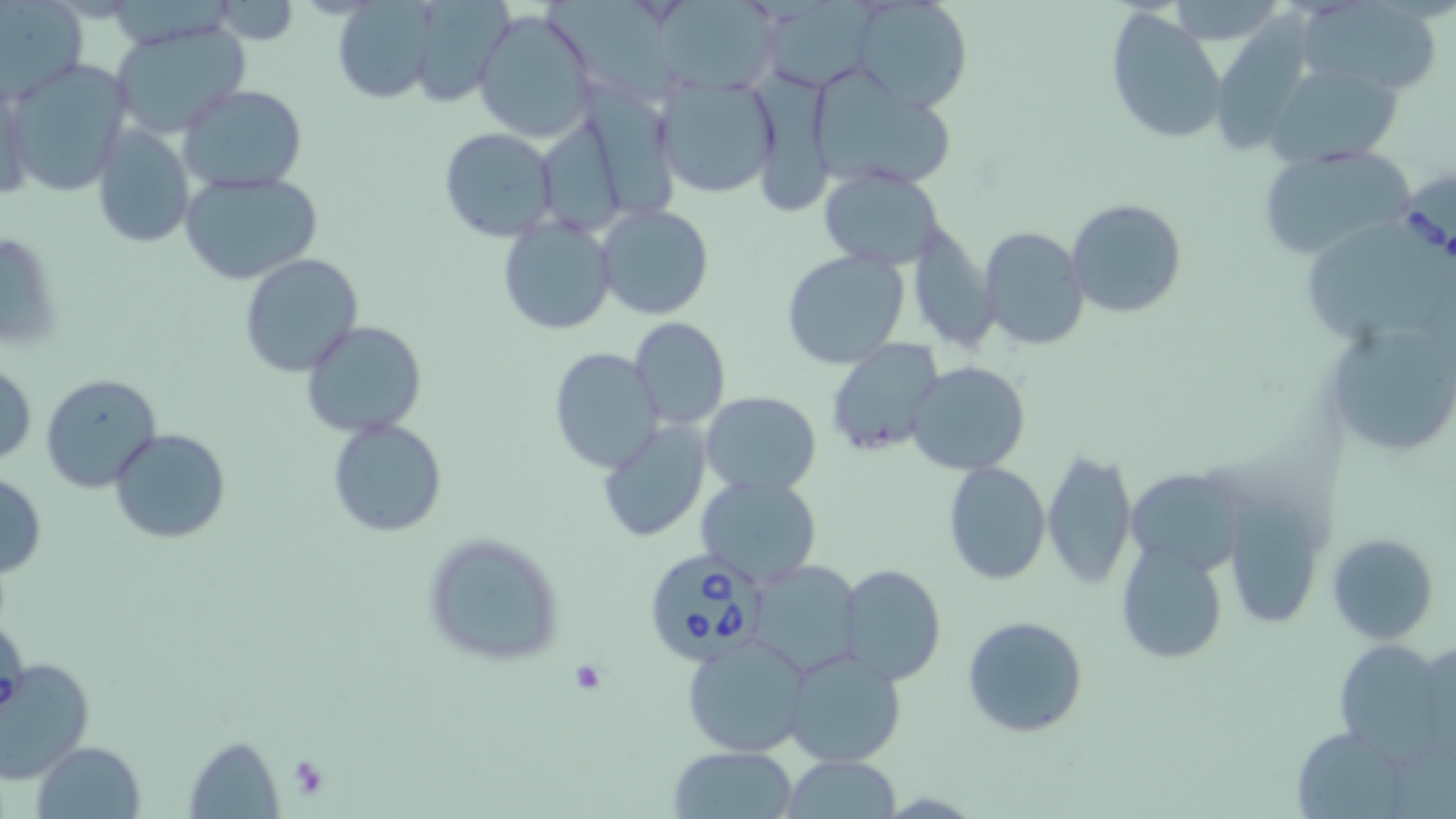
Approximate bounding boxes as (x1, y1, x2, y2) in pixels. Platelet locations: (569, 660, 607, 696), (286, 753, 331, 800). Babesia divergens-infected red blood cell locations: (1399, 173, 1455, 280), (644, 548, 771, 665). Uninfected red blood cell locations: (407, 0, 510, 108), (539, 0, 683, 97), (771, 0, 893, 89), (213, 1, 300, 46), (652, 1, 788, 94), (854, 1, 972, 111), (1, 2, 87, 103), (330, 2, 438, 103), (1162, 2, 1287, 41), (1300, 2, 1443, 96), (472, 7, 598, 142), (1104, 7, 1230, 145), (109, 17, 251, 139), (5, 60, 132, 196), (1268, 62, 1400, 166), (750, 68, 849, 218), (806, 70, 958, 193), (654, 73, 783, 200), (2, 78, 34, 209), (178, 84, 308, 193), (584, 84, 688, 220), (91, 123, 195, 248), (439, 127, 558, 242), (1256, 144, 1414, 260), (818, 168, 946, 269), (178, 169, 324, 286), (1064, 199, 1186, 320), (595, 204, 714, 320), (498, 216, 615, 336), (906, 220, 999, 352), (978, 226, 1089, 351), (1, 227, 61, 353), (781, 249, 909, 369), (240, 254, 363, 376), (628, 316, 731, 431), (1320, 316, 1456, 460), (301, 321, 426, 438), (827, 338, 943, 456), (548, 346, 664, 473), (1, 359, 36, 470), (906, 360, 1033, 476), (39, 373, 161, 493), (700, 391, 821, 495), (328, 418, 447, 537), (597, 418, 711, 543), (110, 428, 231, 545), (1041, 449, 1137, 591), (942, 461, 1052, 585), (1129, 466, 1252, 580), (0, 473, 48, 579), (694, 474, 823, 586), (1220, 491, 1328, 632), (421, 533, 567, 669), (1327, 533, 1439, 644), (1115, 538, 1229, 663), (747, 561, 863, 677), (838, 564, 947, 686), (1, 611, 28, 721), (961, 614, 1091, 738), (681, 634, 812, 757), (1333, 638, 1449, 757), (782, 647, 906, 767), (0, 655, 94, 783), (1296, 725, 1405, 819), (185, 735, 285, 816), (33, 741, 147, 819), (667, 746, 798, 819), (782, 755, 904, 817). Slide-level diagnosis: Babesia divergens. 1000x magnification. Image is 1456×819 pixels. May-Grünwald-Giemsa-stained preparation. Single field of view. Thin blood smear. Optical microscopy.